Describe the morphology of the erythrocytes.
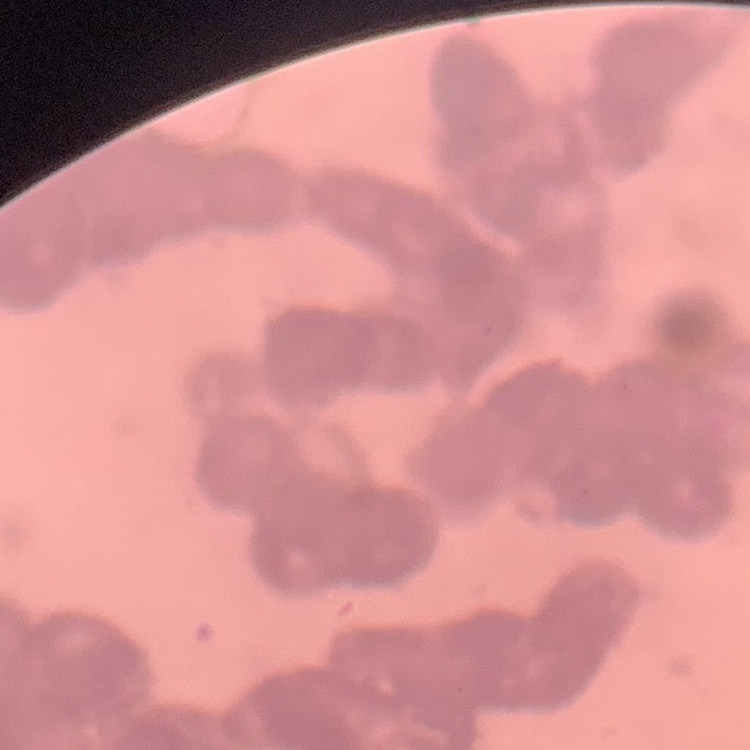

They show rouleaux formation.

One tile cut from a larger photomicrograph. Stained with either Field's or Giemsa. Thin blood smear.